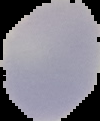

Segmented cell region on a black background. Image is 100×121 pixels. Malaria status: uninfected. From a thin blood smear.